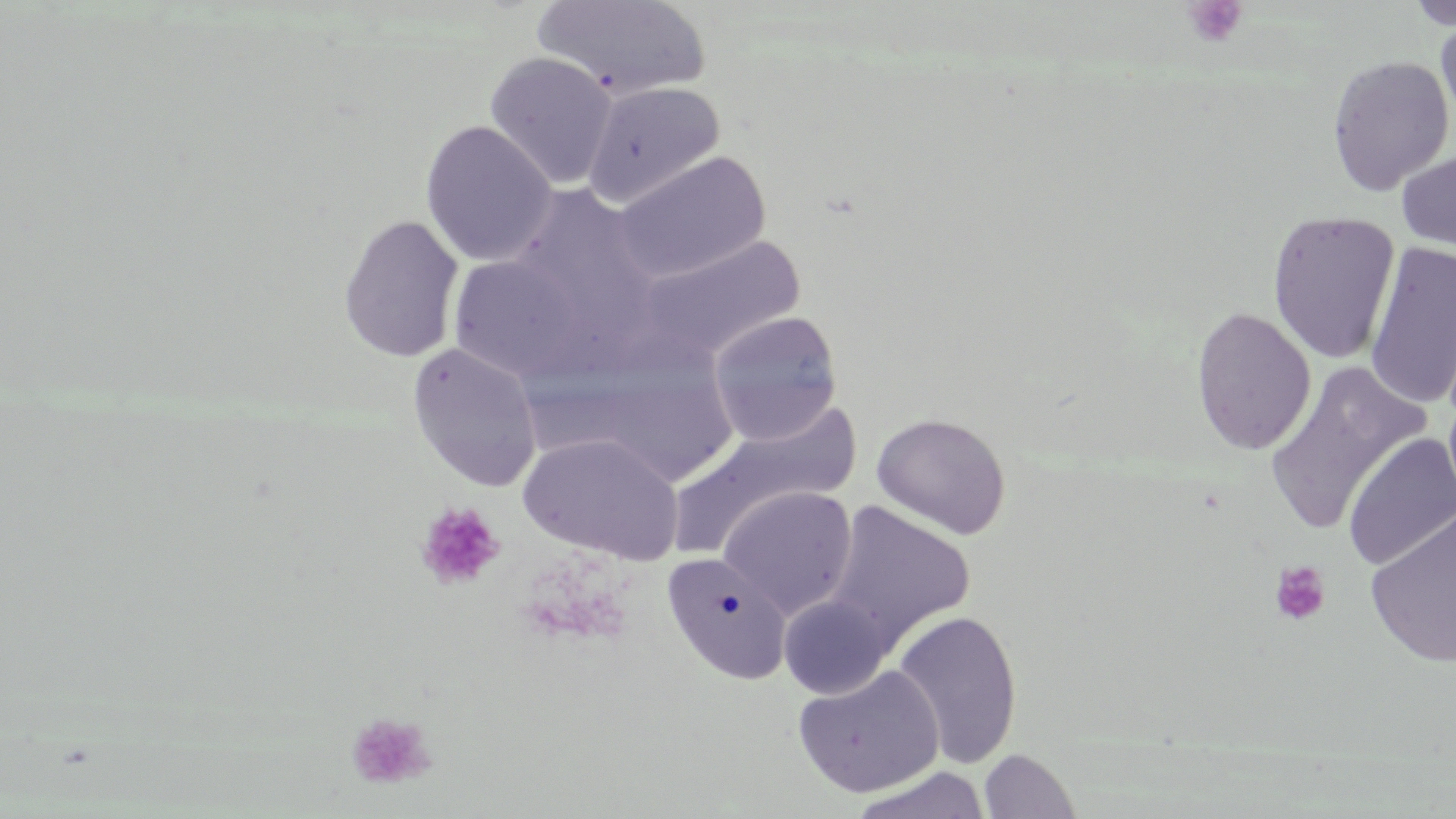
slide-level diagnosis = negative for blood parasites
preparation = thin blood smear
stain = May-Grünwald-Giemsa
uninfected red blood cell locations = approximate bounding boxes as (x1, y1, x2, y2) in pixels: (531, 0, 712, 102), (1401, 0, 1456, 31), (1434, 13, 1456, 128), (484, 51, 617, 190), (1326, 55, 1455, 195), (582, 80, 725, 209), (420, 121, 558, 267), (1396, 147, 1456, 258), (611, 150, 771, 285), (504, 183, 666, 348), (1266, 210, 1401, 364), (338, 214, 464, 363), (635, 233, 805, 363), (1363, 242, 1456, 410), (447, 254, 594, 384), (1190, 305, 1317, 455), (707, 310, 843, 446), (406, 342, 543, 492), (1263, 363, 1432, 535), (669, 405, 863, 554), (872, 412, 1011, 540), (1342, 432, 1456, 571), (518, 433, 684, 565), (717, 485, 858, 619), (824, 501, 975, 649), (1364, 504, 1456, 669), (662, 551, 791, 684), (779, 594, 892, 699), (891, 610, 1022, 769), (792, 664, 944, 798), (979, 748, 1081, 818), (848, 766, 992, 819)
field of view = single
modality = optical microscopy
magnification = 1000x
platelet locations = approximate bounding boxes as (x1, y1, x2, y2) in pixels: (1181, 1, 1248, 48), (414, 501, 506, 590), (1270, 561, 1331, 625), (345, 712, 438, 791)
image size = 1456×819 pixels